Give the extent of all Plasmodium ovale-infected red blood cells.
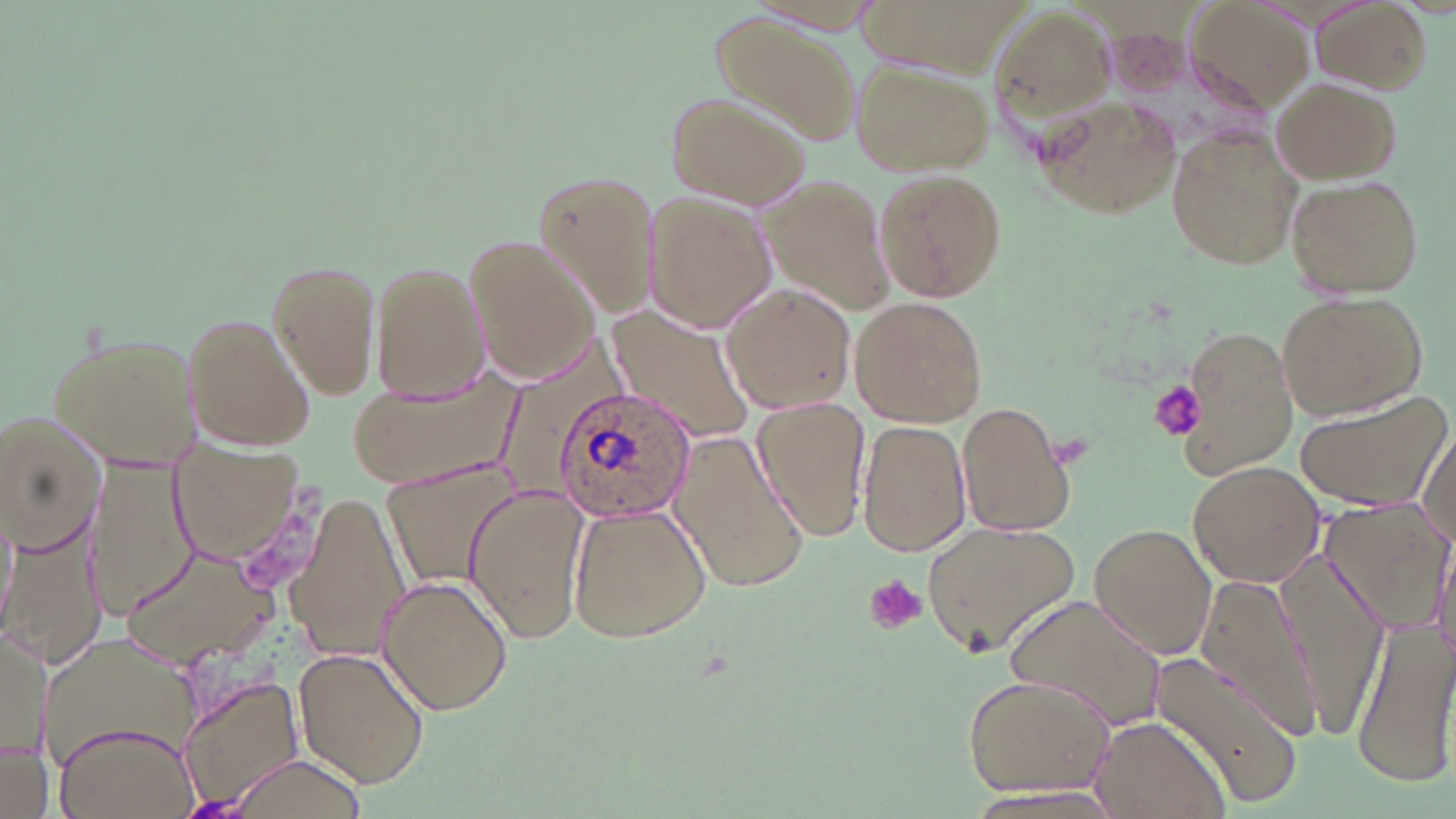

Approximate bounding boxes as [x1, y1, x2, y2] in pixels.
Plasmodium ovale-infected red blood cells: [554, 386, 698, 520].

Summary:
  - Platelet locations: [1152, 381, 1208, 441], [862, 575, 926, 635]
  - Uninfected red blood cell locations: [1186, 0, 1316, 112], [1313, 1, 1431, 96], [989, 4, 1116, 131], [707, 12, 858, 147], [852, 60, 992, 176], [1269, 76, 1400, 185], [665, 87, 812, 209], [1035, 92, 1183, 219], [1166, 124, 1304, 272], [531, 165, 663, 320], [872, 169, 1009, 302], [756, 173, 893, 309], [1287, 173, 1425, 298], [644, 198, 776, 332], [465, 232, 605, 384], [266, 258, 382, 399], [370, 260, 491, 402], [719, 282, 855, 415], [1276, 291, 1428, 422], [848, 297, 989, 427], [605, 309, 753, 442], [182, 312, 316, 452], [1167, 323, 1299, 482], [45, 326, 205, 469], [348, 374, 515, 488], [1294, 388, 1454, 513], [750, 397, 870, 544], [957, 401, 1076, 538], [2, 413, 108, 552], [855, 419, 971, 555], [1417, 423, 1453, 545], [670, 429, 812, 591], [169, 446, 303, 565], [85, 456, 200, 620], [1186, 460, 1326, 589], [382, 462, 517, 586], [462, 484, 590, 644], [284, 493, 410, 661], [1322, 499, 1452, 630], [566, 501, 713, 644], [1, 506, 18, 631], [7, 509, 107, 675], [920, 517, 1083, 658], [1089, 524, 1217, 658], [1430, 530, 1456, 666], [1275, 545, 1396, 731], [119, 546, 278, 664], [373, 575, 514, 715], [1191, 575, 1329, 740], [1006, 591, 1168, 731], [2, 618, 47, 773], [1351, 621, 1456, 790], [39, 629, 207, 781], [293, 647, 429, 787], [1148, 648, 1302, 810], [961, 674, 1117, 798], [179, 677, 305, 813], [1084, 715, 1229, 819], [54, 720, 198, 819], [1, 742, 51, 819], [224, 751, 370, 819], [955, 783, 1129, 818]
  - Slide-level diagnosis: Plasmodium ovale
  - Preparation: thin blood smear
  - Image size: 1456×819 pixels
  - Stain: May-Grünwald-Giemsa
  - Field of view: one of a larger specimen
  - Magnification: 1000x
  - Modality: light microscopy